Assess the morphology of the red blood cells.
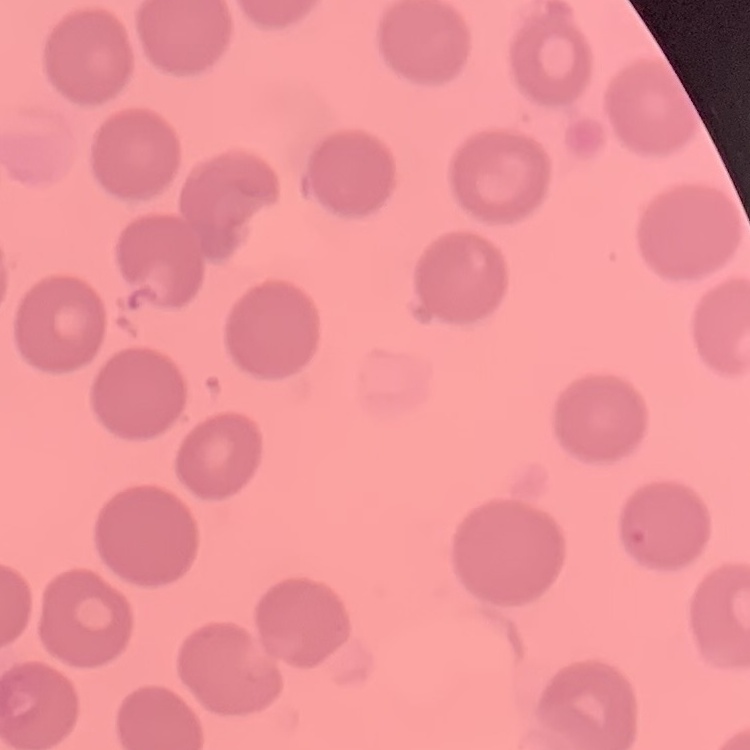

No rouleaux formation.

Field's or Giemsa stain. Thin peripheral smear. One tile cut from a larger photomicrograph.